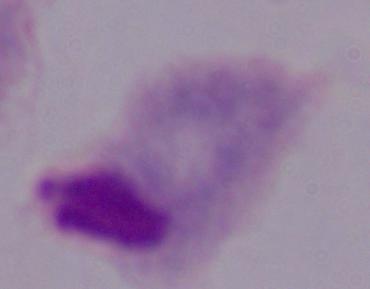 A trichomonad is shown. 1000x magnification. Photomicrograph.